State which parasite is depicted.
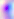

This is Toxoplasma gondii.

Summary:
  - Modality: micrograph
  - Magnification: 400x